State the blood parasite species.
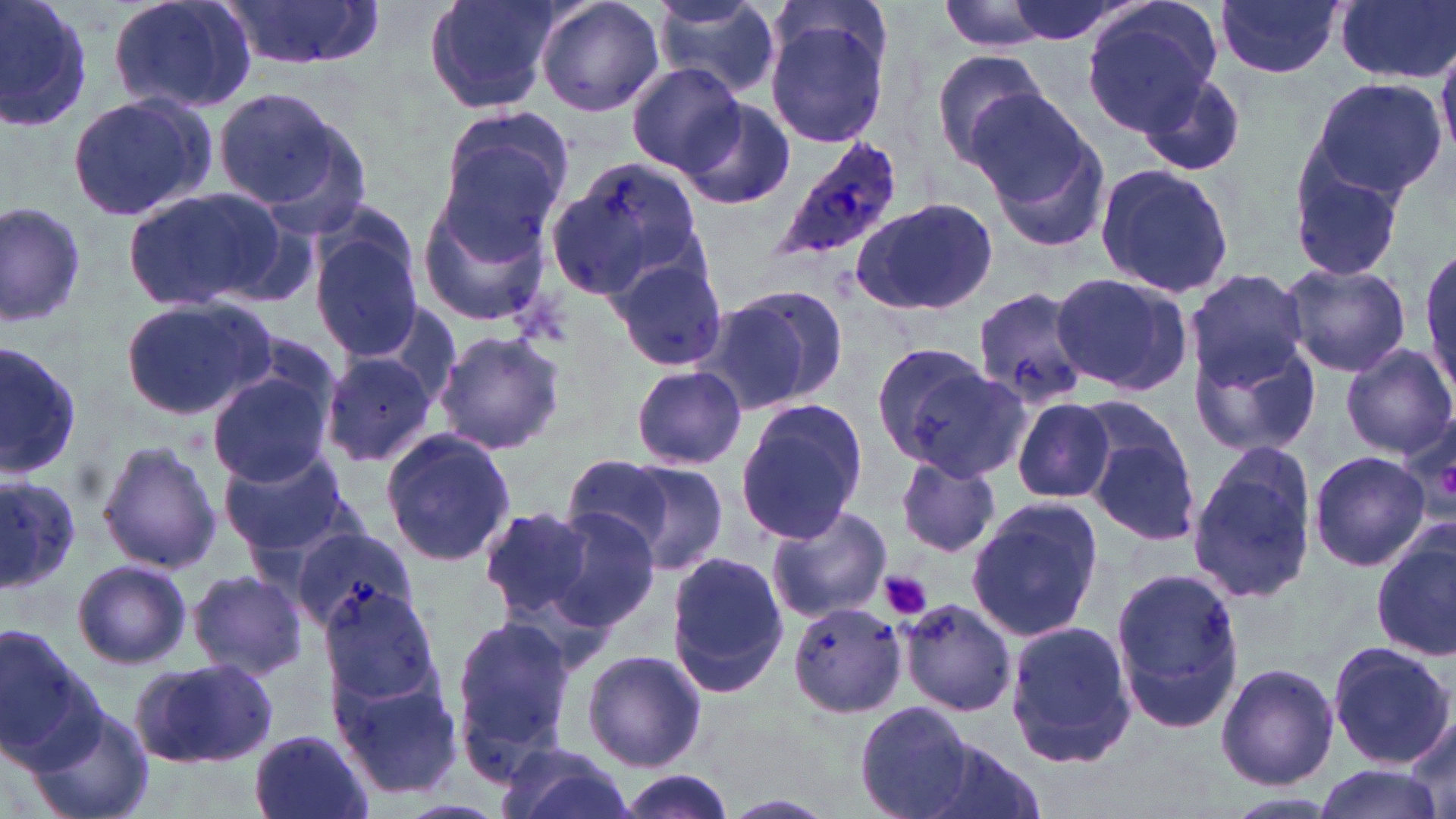

Plasmodium ovale.

Summary:
  - Coordinate format: approximate bounding boxes as (x1,y1)-(x2,y2) corner pairs in pixels
  - Platelet locations: (881,571)-(932,620)
  - Uninfected red blood cell locations: (0,0)-(95,137), (106,0)-(258,114), (424,0)-(562,113), (534,0)-(665,118), (998,0)-(1134,45), (1217,0)-(1343,79), (1333,0)-(1456,85), (651,1)-(781,97), (936,1)-(1066,53), (1081,1)-(1221,135), (223,2)-(380,74), (766,14)-(889,152), (930,47)-(1053,168), (627,64)-(742,175), (1139,70)-(1247,177), (1306,77)-(1447,201), (212,86)-(350,212), (66,93)-(219,221), (678,99)-(797,212), (974,99)-(1107,247), (441,106)-(578,228), (547,154)-(705,299), (1284,156)-(1409,282), (1093,162)-(1239,300), (416,185)-(557,327), (121,187)-(292,313), (849,196)-(999,317), (1,201)-(88,332), (309,223)-(425,361), (607,253)-(730,374), (1280,261)-(1411,378), (1183,267)-(1311,387), (1048,272)-(1190,395), (710,284)-(852,413), (970,286)-(1091,411), (119,297)-(274,422), (1189,323)-(1319,459), (433,330)-(567,456), (864,338)-(1005,471), (0,341)-(81,482), (1337,344)-(1455,460), (320,352)-(441,468), (630,365)-(746,471), (207,368)-(336,488), (1008,395)-(1118,503), (1071,396)-(1187,494), (734,399)-(870,546), (1081,415)-(1204,549), (379,428)-(515,570), (95,439)-(222,575), (1185,443)-(1316,606), (218,447)-(356,558), (1309,449)-(1430,571), (561,454)-(683,559), (895,454)-(1000,559), (605,459)-(731,575), (0,475)-(82,592), (965,497)-(1106,641), (535,505)-(662,631), (764,505)-(893,624), (477,507)-(593,623), (288,524)-(418,635), (1372,532)-(1456,663), (664,551)-(790,695), (71,559)-(192,670), (1110,566)-(1244,736), (186,569)-(308,681), (321,578)-(446,714), (898,598)-(1018,718), (788,602)-(908,719), (449,612)-(580,777), (1004,622)-(1138,770), (0,626)-(97,763), (1326,642)-(1453,767), (580,648)-(707,774), (131,659)-(280,770), (1216,663)-(1339,791), (331,666)-(463,801), (853,700)-(977,819), (26,702)-(156,819), (1402,713)-(1455,816), (249,729)-(377,819), (928,740)-(1046,819), (492,742)-(635,819), (1310,764)-(1443,819), (613,770)-(736,819), (1221,791)-(1342,818)
  - Plasmodium ovale-infected red blood cell locations: (767,136)-(904,270)
  - Image size: 1456×819 pixels
  - Field of view: one of a larger specimen
  - Magnification: 1000x
  - Stain: May-Grünwald-Giemsa
  - Modality: optical microscopy
  - Preparation: thin blood film